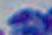
Summary:
  - Magnification: 1000x
  - Modality: micrograph
  - Identification: Toxoplasma gondii